State which parasite is depicted.
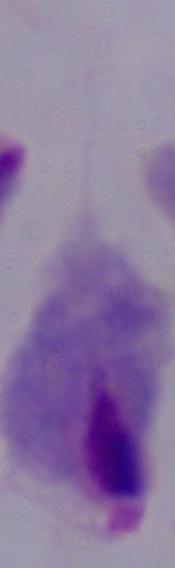

A trichomonad.

Micrograph. 1000x magnification.